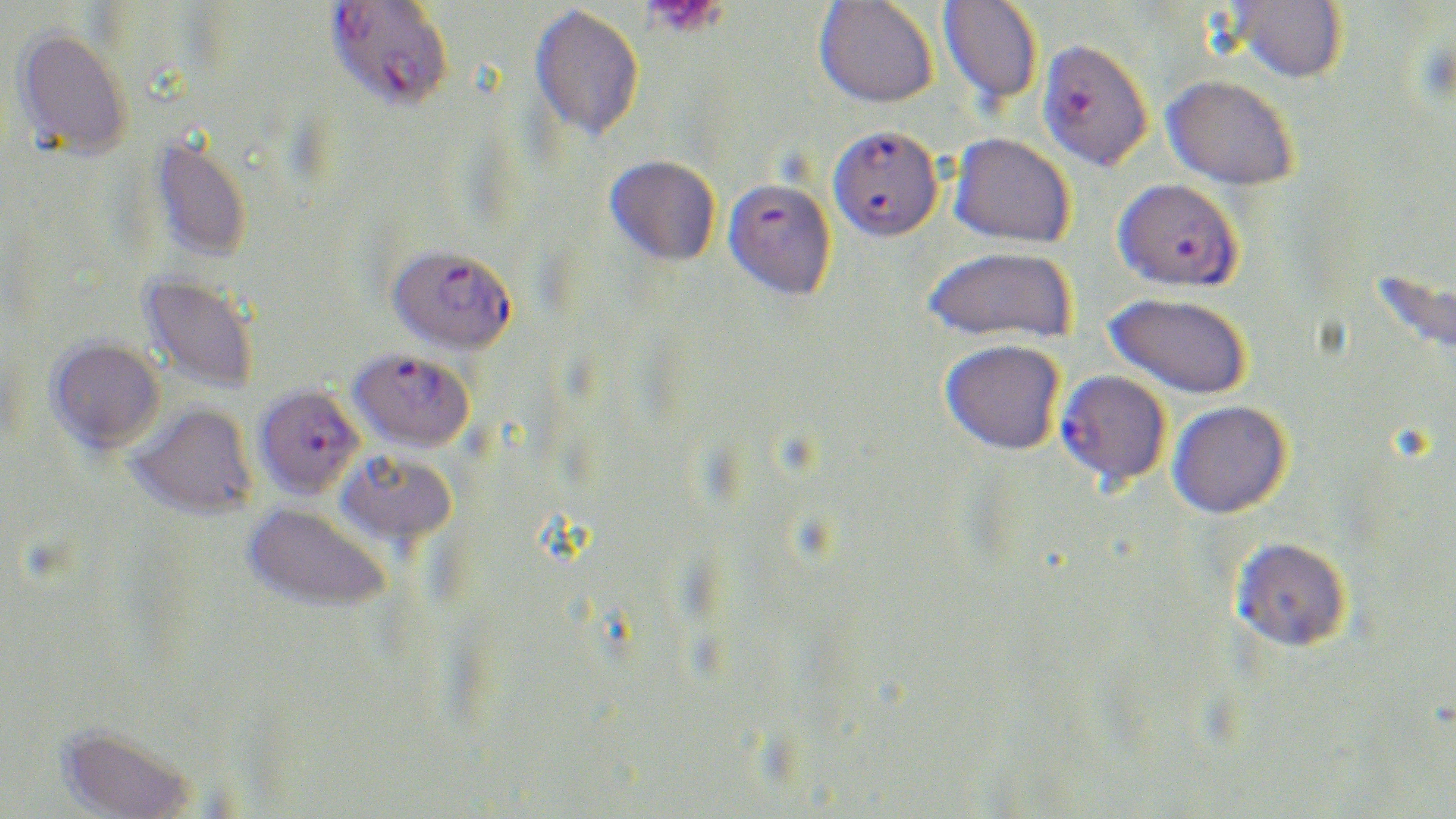
Plasmodium falciparum-infected red blood cell locations = approximate bounding boxes as (x1, y1, x2, y2) in pixels: (325, 1, 454, 110), (1036, 40, 1154, 173), (828, 127, 944, 245), (723, 178, 838, 302), (1112, 180, 1243, 295), (387, 244, 518, 354), (348, 347, 475, 452), (1054, 370, 1171, 490), (254, 384, 365, 499)
slide-level diagnosis = Plasmodium falciparum
field of view = single
image size = 1456×819 pixels
preparation = thin blood smear
magnification = 1000x
uninfected red blood cell locations = approximate bounding boxes as (x1, y1, x2, y2) in pixels: (814, 0, 938, 110), (938, 0, 1042, 107), (1222, 1, 1347, 87), (530, 4, 645, 140), (12, 26, 134, 161), (1160, 75, 1299, 194), (151, 134, 252, 263), (948, 134, 1074, 249), (604, 154, 721, 266), (923, 248, 1077, 347), (139, 272, 260, 394), (1103, 294, 1251, 402), (47, 337, 165, 454), (940, 341, 1065, 458), (1167, 401, 1292, 521), (127, 402, 258, 520), (335, 450, 458, 548), (243, 502, 392, 613), (1230, 538, 1352, 654), (55, 724, 200, 819)
platelet locations = approximate bounding boxes as (x1, y1, x2, y2) in pixels: (644, 0, 726, 38)
stain = May-Grünwald-Giemsa
modality = light microscopy